State which parasite is depicted.
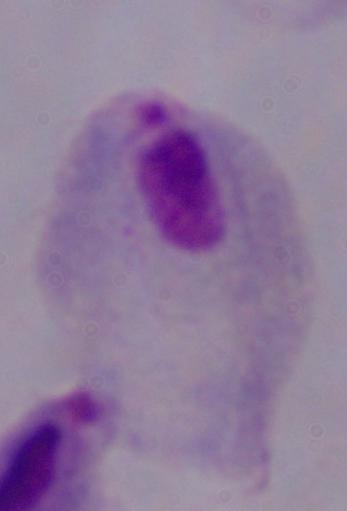
A trichomonad.

Micrograph. Captured at 1000x magnification.